State which parasite is depicted.
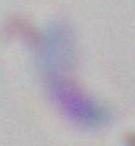

This is Toxoplasma gondii.

Summary:
  - Magnification: 1000x
  - Modality: photomicrograph